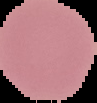 Cell region segmented out of the field of view; the surrounding area is masked to black. Malaria status: uninfected. From a thin blood film. Image is 97×103 pixels.